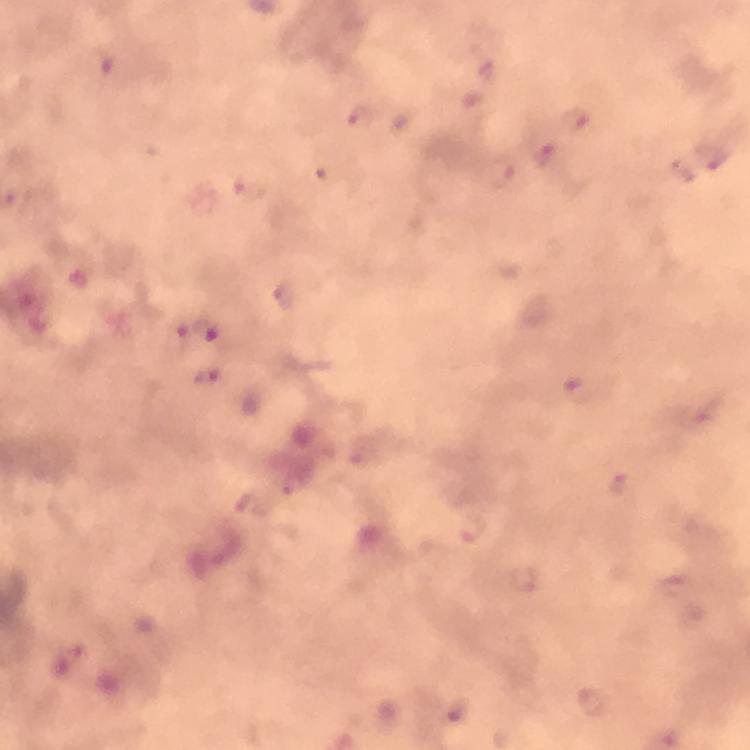
Approximate centers as (x, y) in pixels.
Summary:
  - Plasmodium parasite locations: (473, 103), (361, 116), (576, 118), (545, 154), (710, 157), (501, 173), (208, 327), (579, 390), (471, 528), (593, 702)
  - Capture: smartphone photograph through a microscope
  - Image size: 750×750 pixels
  - Immersion oil: applied
  - Magnification: 100x
  - Context: from a malaria diagnostic workup
  - Cropped from: one field of view
  - Stain: Giemsa
  - Preparation: thick blood smear